Name the parasite shown.
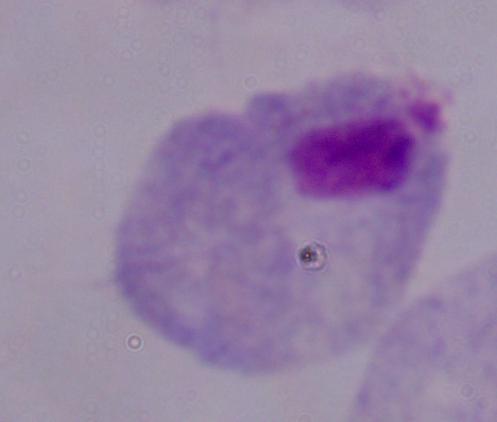

A trichomonad.

Summary:
  - Magnification: 1000x
  - Modality: photomicrograph